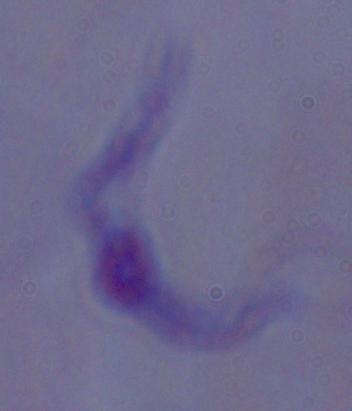 A trypanosome is seen. Captured at 1000x magnification. Photomicrograph.